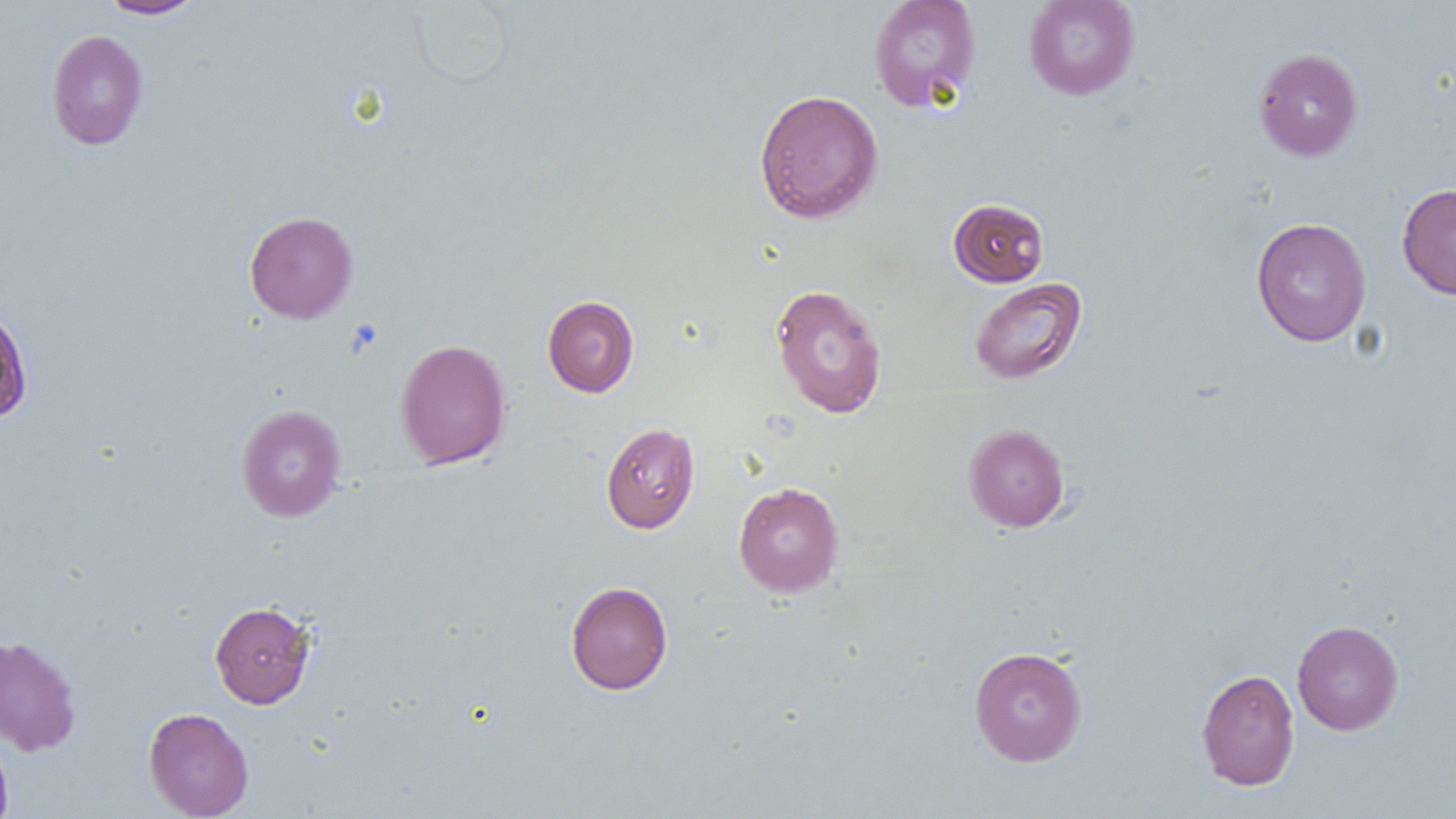
Summary:
  - Coordinate format: approximate bounding boxes as (x1,y1)-(x2,y2) corner pairs in pixels
  - Uninfected red blood cell locations: (98,0)-(205,19), (868,0)-(982,112), (1023,0)-(1140,101), (46,30)-(148,150), (1253,47)-(1363,161), (754,89)-(884,223), (1396,182)-(1456,299), (948,198)-(1049,287), (244,211)-(358,323), (1251,217)-(1372,347), (969,277)-(1087,385), (769,283)-(888,419), (542,295)-(639,398), (0,304)-(34,425), (395,338)-(511,470), (236,404)-(346,523), (601,422)-(700,533), (963,423)-(1070,533), (733,481)-(844,596), (565,581)-(673,695), (209,601)-(316,708), (1292,619)-(1404,735), (0,633)-(82,756), (969,645)-(1087,766), (1196,668)-(1300,791), (143,707)-(254,819), (0,731)-(14,819)
  - Platelet locations: (346,318)-(384,357)
  - Slide-level diagnosis: no evidence of blood parasites
  - Magnification: 1000x
  - Image size: 1456×819 pixels
  - Preparation: thin blood smear
  - Modality: optical microscopy
  - Field of view: single